Describe the morphology of the erythrocytes.
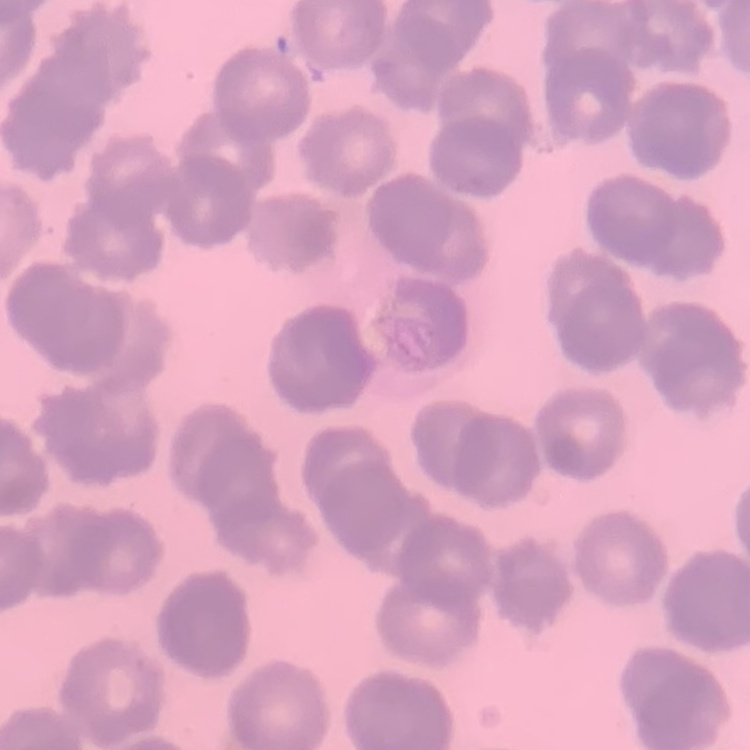

Rouleaux formation.

Summary:
  - Image type: one tile cut from a larger photomicrograph
  - Preparation: thin peripheral smear
  - Stain: Field's or Giemsa